Point out each Plasmodium parasite.
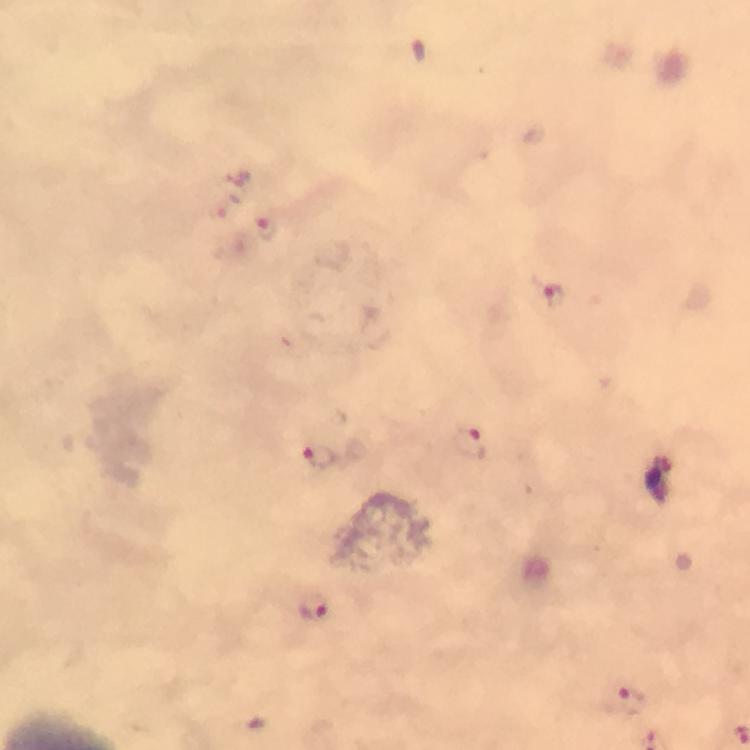
Approximate centers as {x, y} in pixels.
Plasmodium parasites: {238, 177}, {224, 206}, {267, 230}, {553, 296}, {470, 444}, {318, 455}, {312, 606}, {626, 700}.

capture = smartphone camera through the microscope
preparation = thick smear
cropped from = one field of view
image size = 750×750 pixels
magnification = 100x
context = from a malaria diagnostic workup
immersion oil = used
stain = Giemsa